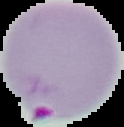

Summary:
  - Image type: segmented cell region with the area outside set to black
  - Image size: 124×127 pixels
  - Malaria status: parasitized
  - Preparation: thin blood film